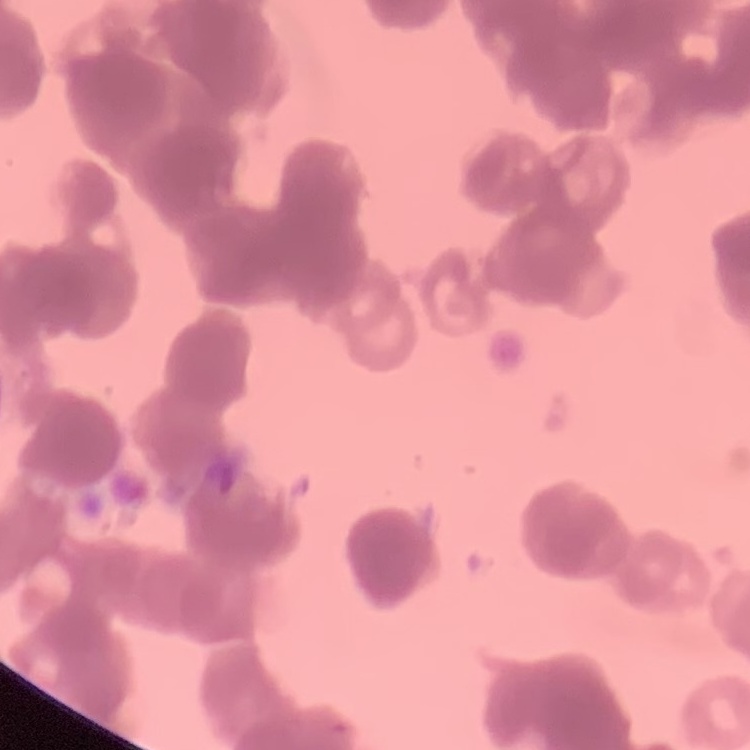

The erythrocytes exhibit rouleaux formation. Stained with either Field's or Giemsa. One tile cut from a larger photomicrograph. Thin blood smear.